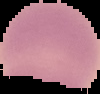

image type = cell region segmented out of the field of view; surrounding area masked to black
preparation = thin blood smear
image size = 100×94 pixels
malaria status = uninfected